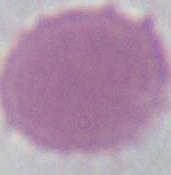
Summary:
  - Identification: erythrocyte
  - Magnification: 1000x
  - Modality: photomicrograph